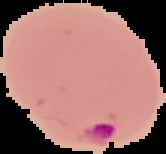
Malaria status: parasitized. Image is 166×154 pixels. Segmented cell region on a black background. From a thin blood film.